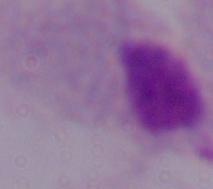

{
  "modality": "photomicrograph",
  "identification": "trichomonad",
  "magnification": "1000x"
}